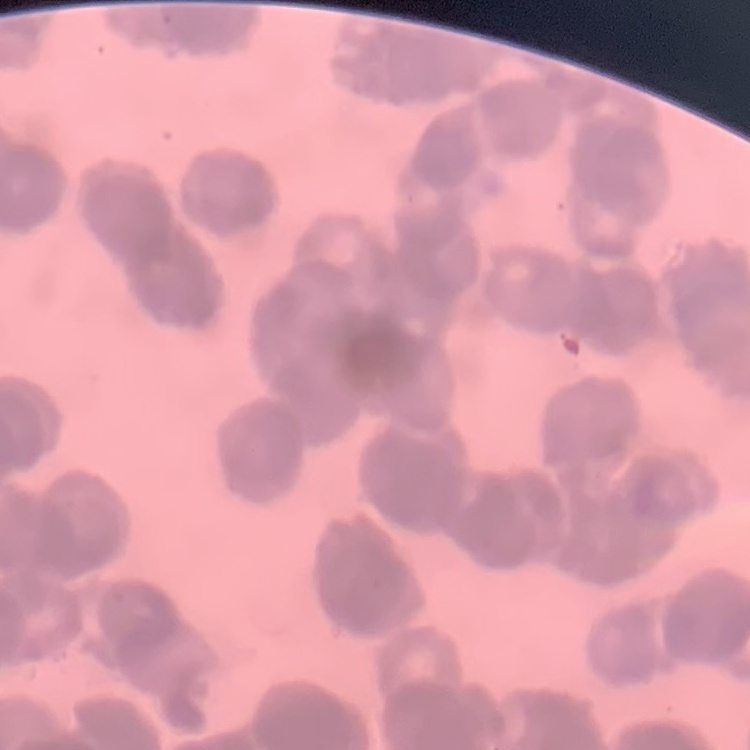

Summary:
  - Erythrocyte morphology: rouleaux formation
  - Preparation: thin blood film
  - Image type: square crop of a larger photomicrograph
  - Stain: Field's or Giemsa